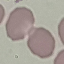
Result: no malaria parasites seen. Cell patch, automatically extracted from a larger field of view and resized to 64 × 64 pixels. Thin smear of blood. Giemsa stain. Acquired by smartphone through the microscope eyepiece.